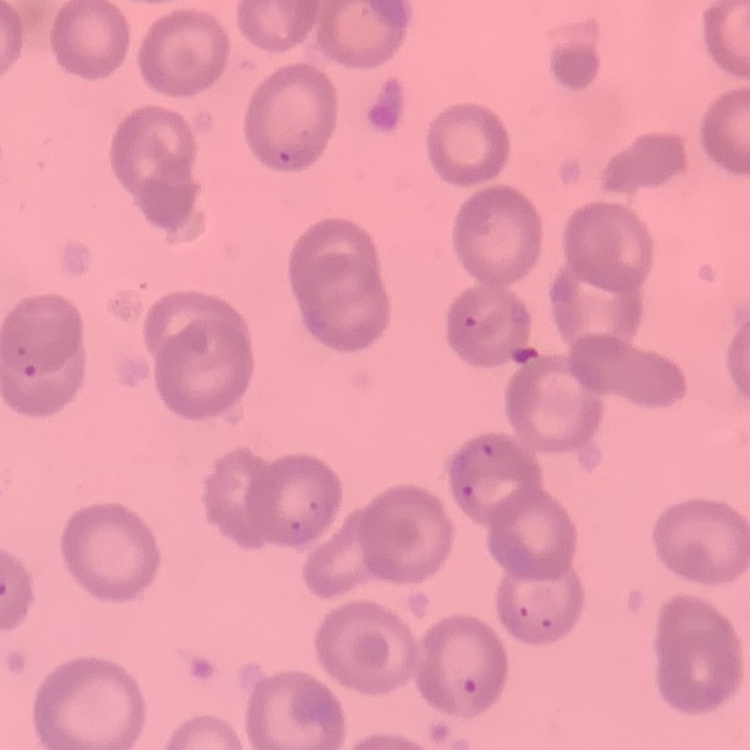
Summary:
  - Red blood cell morphology: no rouleaux formation
  - Preparation: thin peripheral smear
  - Stain: Field's or Giemsa
  - Image type: square crop of a larger photomicrograph